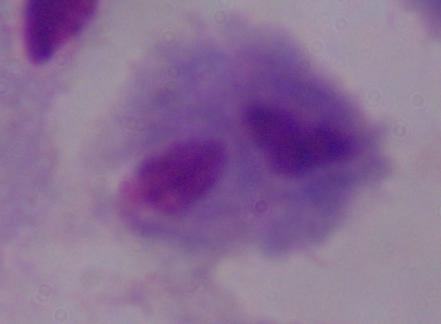

{
  "modality": "micrograph",
  "identification": "trichomonad",
  "magnification": "1000x"
}